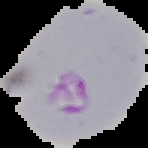
result: Plasmodium parasites identified
image_size: 148×148 pixels
image_type: segmented cell region with the area outside set to black
preparation: thin blood film